Comment on the morphology of the erythrocytes.
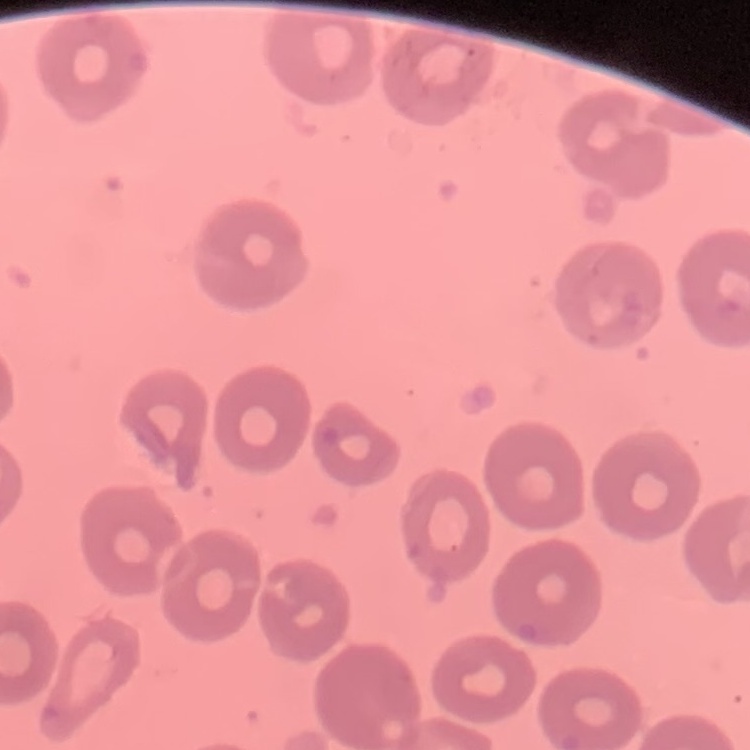
They show no rouleaux formation.

Summary:
  - Stain: Field's or Giemsa
  - Preparation: thin blood film
  - Image type: square crop of a larger photomicrograph